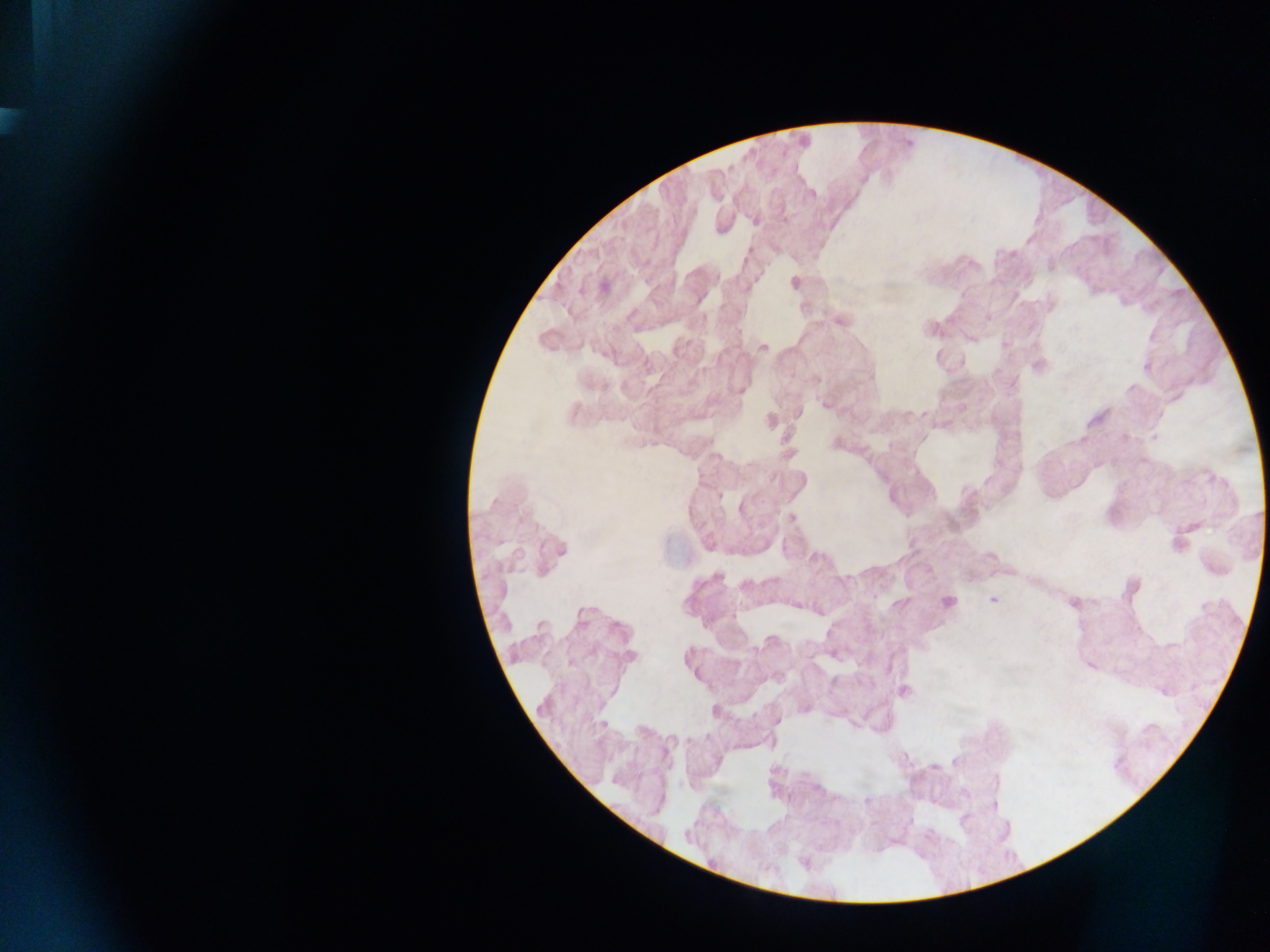

Approximate centers as (x, y) in pixels.
Summary:
  - Plasmodium parasite locations: (754, 219), (794, 282), (603, 287), (840, 319), (932, 328), (763, 346), (1037, 366), (1148, 366), (740, 391), (826, 405), (797, 413), (770, 421), (789, 453), (791, 517), (1179, 542), (556, 551), (717, 577), (1131, 587), (993, 599), (947, 601), (1073, 604), (630, 656), (1090, 665), (903, 691), (805, 707), (776, 720), (993, 804)
  - Image size: 1270×952 pixels
  - Country: Ghana
  - Preparation: thick blood film
  - Field of view: single
  - Capture: mobile-phone photograph through a microscope